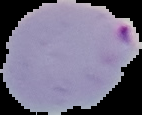
Summary:
  - Malaria status: parasitized
  - Image type: segmented cell region with the area outside set to black
  - Image size: 142×115 pixels
  - Preparation: thin blood smear